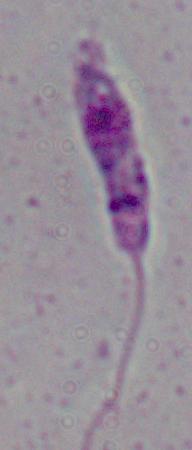
Summary:
  - Modality: micrograph
  - Identification: Leishmania
  - Magnification: 1000x